State which parasite is depicted.
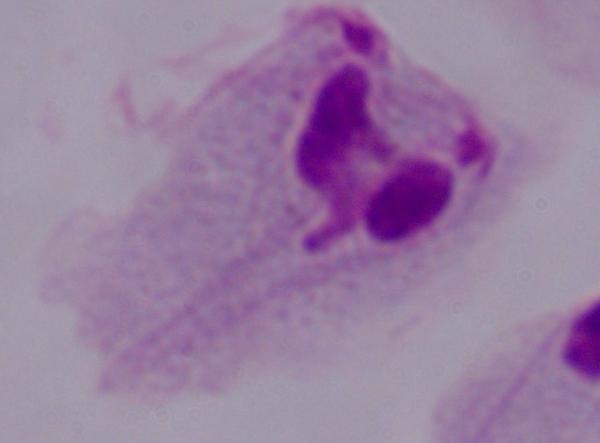

This is a trichomonad.

Micrograph. Captured at 1000x magnification.